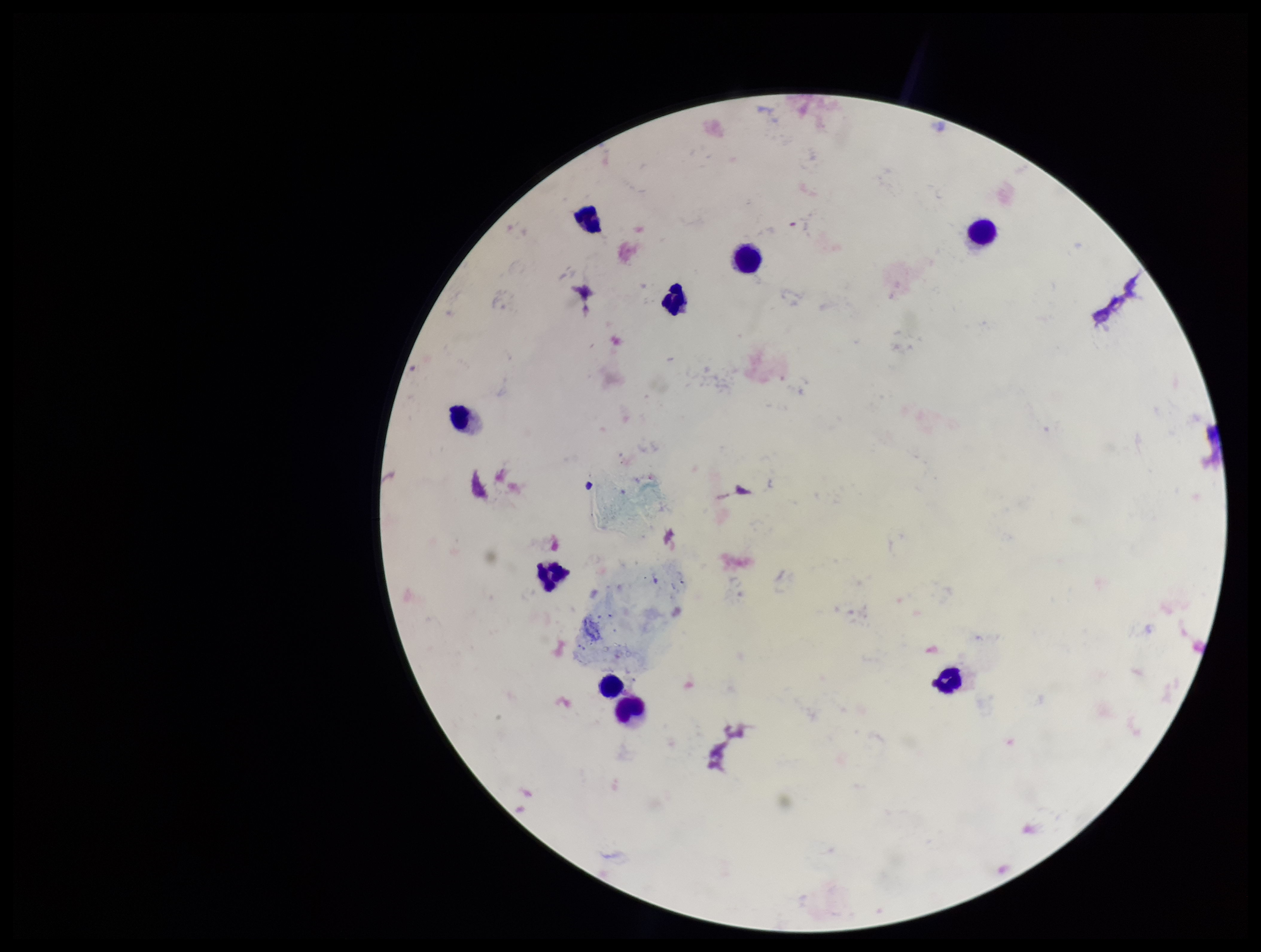
patient malaria status = negative
field of view = one from this slide
stain = Giemsa
parasite count = 0
capture = smartphone photograph through the microscope eyepiece
leukocyte count = 9
image size = 1261×952 pixels
Plasmodium parasites = none identified
preparation = thick